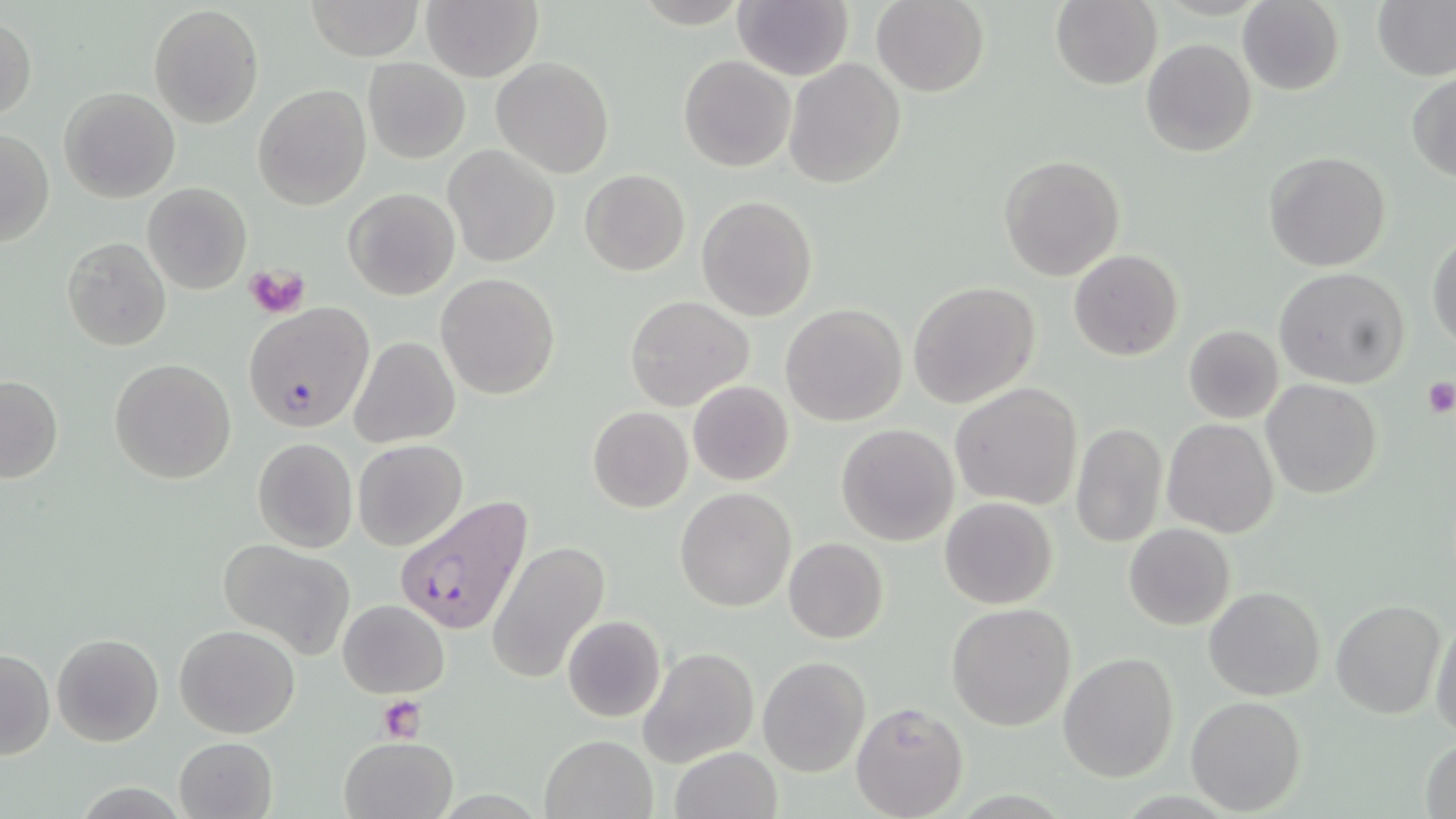

Approximate bounding boxes as (x1,y1)-(x2,y2) corner pairs in pixels. Platelet locations: (245,263)-(311,319), (1418,376)-(1455,418), (377,697)-(428,740). Uninfected red blood cell locations: (305,0)-(424,61), (1050,0)-(1161,90), (1373,0)-(1455,82), (421,1)-(542,81), (870,1)-(989,95), (1236,1)-(1345,94), (733,2)-(851,80), (148,5)-(265,129), (0,16)-(36,123), (1141,38)-(1257,157), (678,55)-(794,172), (491,56)-(616,178), (363,58)-(470,163), (784,59)-(905,188), (1407,72)-(1456,182), (253,83)-(372,211), (59,86)-(180,202), (1,126)-(54,248), (444,145)-(560,266), (1264,150)-(1391,272), (999,155)-(1125,280), (579,169)-(690,276), (142,182)-(252,295), (342,187)-(460,301), (93,190)-(216,313), (697,195)-(818,321), (1428,233)-(1456,349), (62,236)-(172,351), (1068,249)-(1183,361), (1273,267)-(1411,388), (436,273)-(561,400), (907,281)-(1041,408), (624,295)-(754,411), (244,302)-(375,433), (781,304)-(907,426), (1183,325)-(1284,423), (350,337)-(460,448), (109,357)-(237,483), (1,376)-(63,484), (1262,379)-(1381,498), (688,381)-(794,485), (949,382)-(1084,510), (588,407)-(693,512), (1162,418)-(1282,537), (1070,422)-(1167,550), (835,424)-(959,547), (251,438)-(358,554), (352,439)-(467,551), (676,488)-(795,611), (940,497)-(1057,609), (1125,523)-(1235,631), (216,538)-(358,658), (784,538)-(889,643), (486,539)-(611,684), (1204,585)-(1325,699), (338,600)-(450,698), (1331,600)-(1445,718), (947,604)-(1077,731), (561,614)-(667,723), (1430,618)-(1456,740), (175,624)-(300,739), (51,633)-(164,747), (639,647)-(758,766), (0,648)-(54,760), (1059,651)-(1179,781), (757,656)-(869,775), (1185,695)-(1307,815), (850,700)-(969,819), (541,734)-(656,818), (339,735)-(457,819), (1419,735)-(1456,819), (173,736)-(278,819), (667,747)-(783,819). Plasmodium falciparum-infected red blood cell locations: (393,495)-(532,636). Slide-level diagnosis: Plasmodium falciparum. Thin blood smear. Single field of view. 1000x magnification. Image is 1456×819 pixels. May-Grünwald-Giemsa-stained preparation. Optical microscopy.